Report the malaria status of this cell.
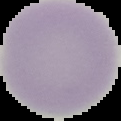

It is uninfected.

{
  "image_size": "121×121 pixels",
  "image_type": "segmented cell region on a black background",
  "preparation": "thin blood film"
}